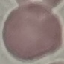

malaria_status: uninfected
capture: smartphone camera at the microscope eyepiece
stain: Giemsa
image_type: automatically extracted cell patch, resized to 64 × 64 pixels
preparation: thin blood film